Give the position of every Plasmodium parasite visible.
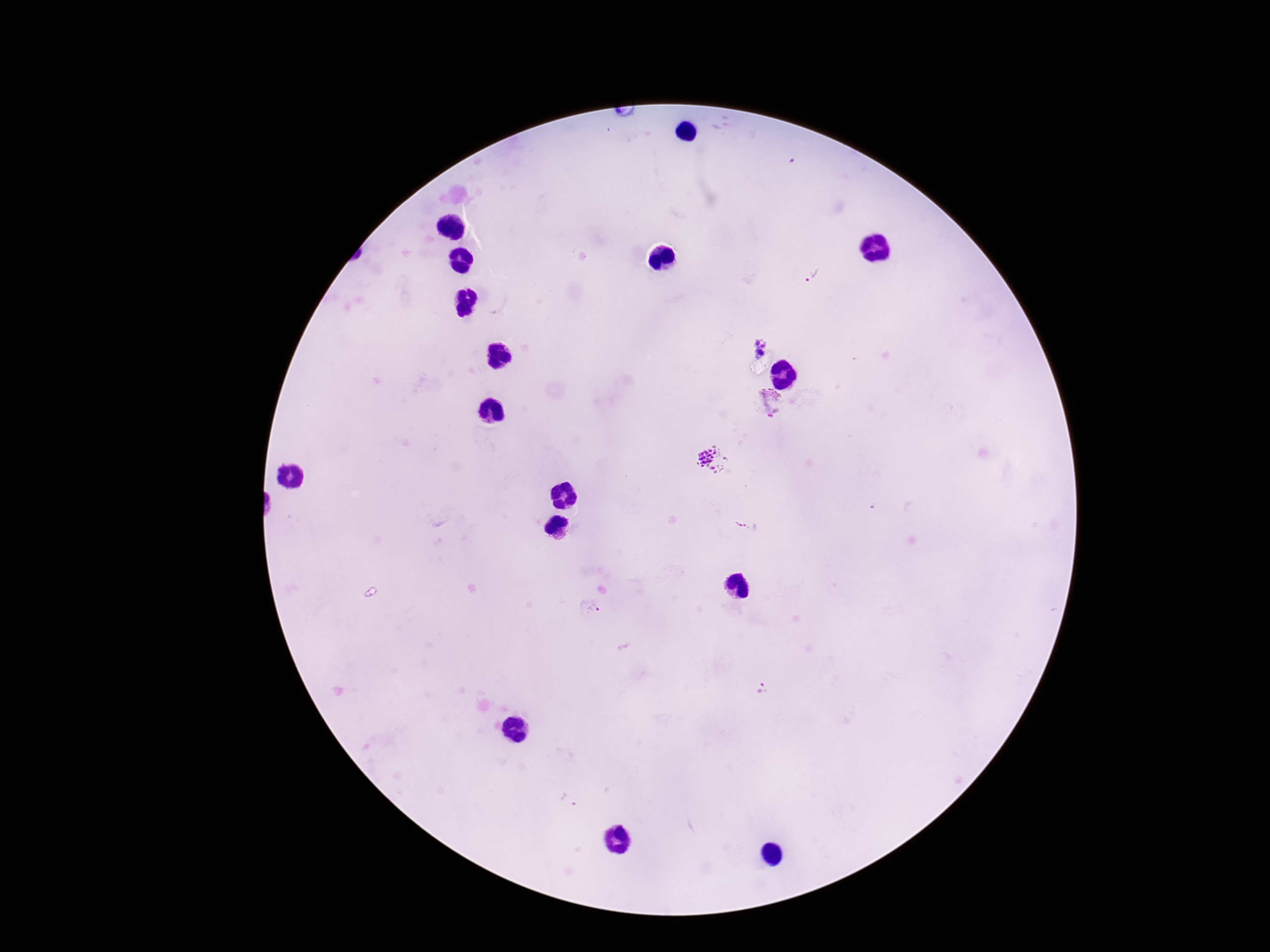

Approximate centers as (x, y) in pixels.
Plasmodium parasites: (816, 273), (758, 345), (769, 402), (712, 459), (746, 526).

Photographed through the microscope eyepiece with a smartphone camera. One field from this slide. Giemsa-stained preparation. Patient malaria status: infected. Thick peripheral-blood smear. Image is 1270×952 pixels. 100x magnification.